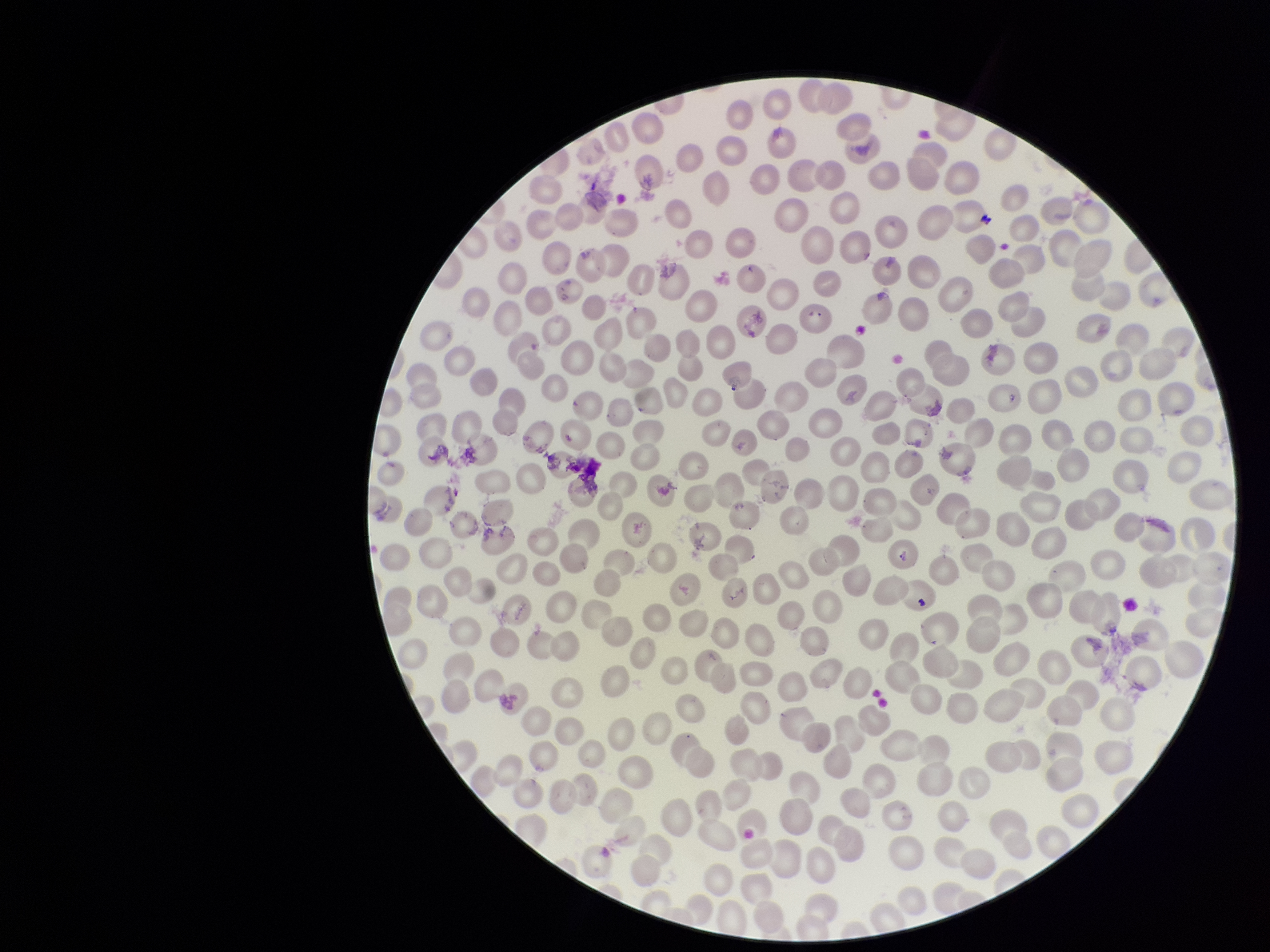
Parasitized red blood cells: none seen. Photographed through the microscope eyepiece with a smartphone camera. One field from this slide. Parasitized red blood cell count: 0. Image is 1270×952 pixels. Patient malaria status: negative. Giemsa stain. Red blood cell count: 290. Preparation: thin.